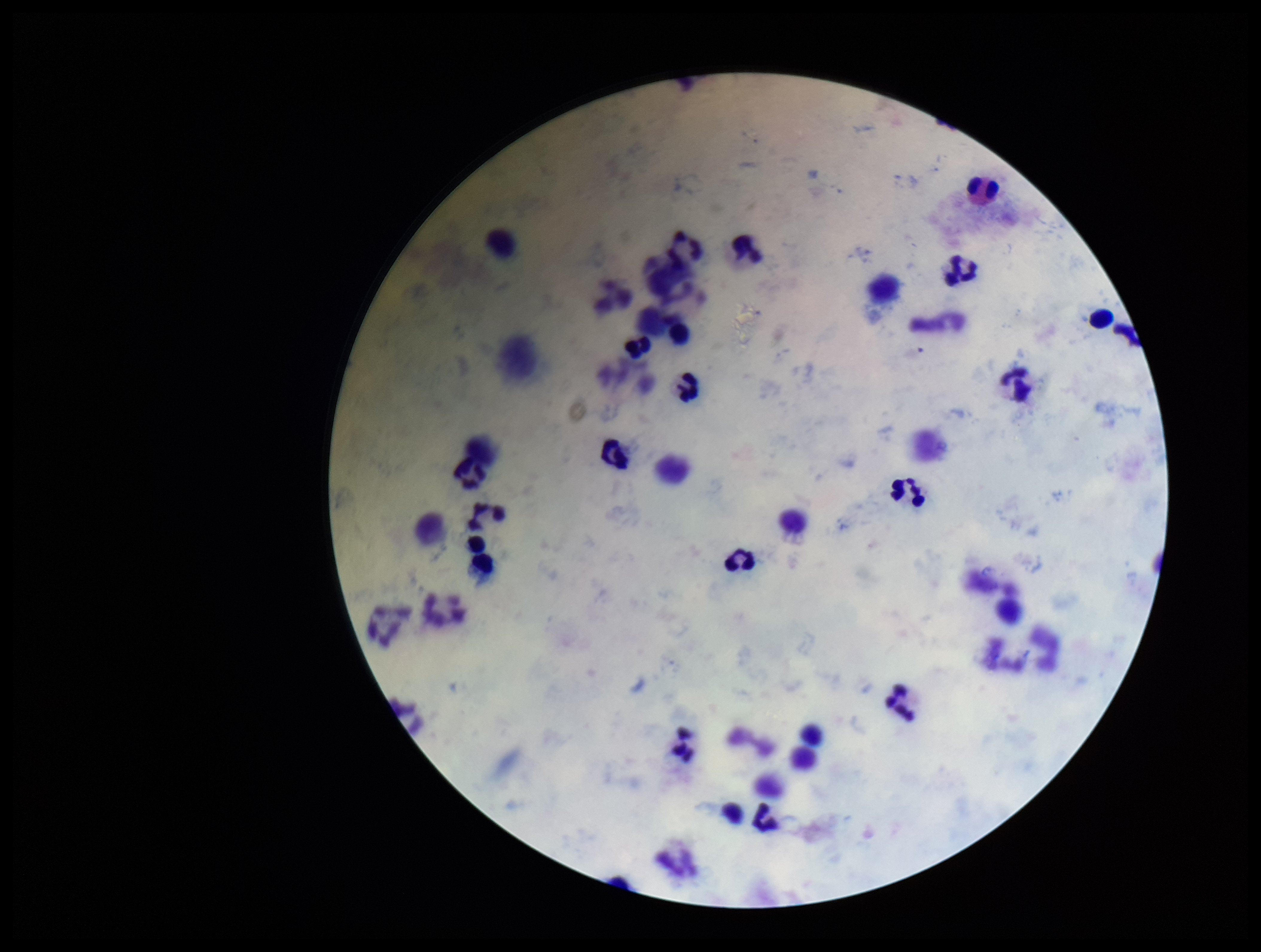
Summary:
  - Capture: smartphone photograph through the microscope eyepiece
  - Image size: 1261×952 pixels
  - Field of view: one from this slide
  - Parasite count: 0
  - Leukocyte count: 43
  - Preparation: thick
  - Patient malaria status: negative
  - Stain: Giemsa
  - Plasmodium parasites: none seen